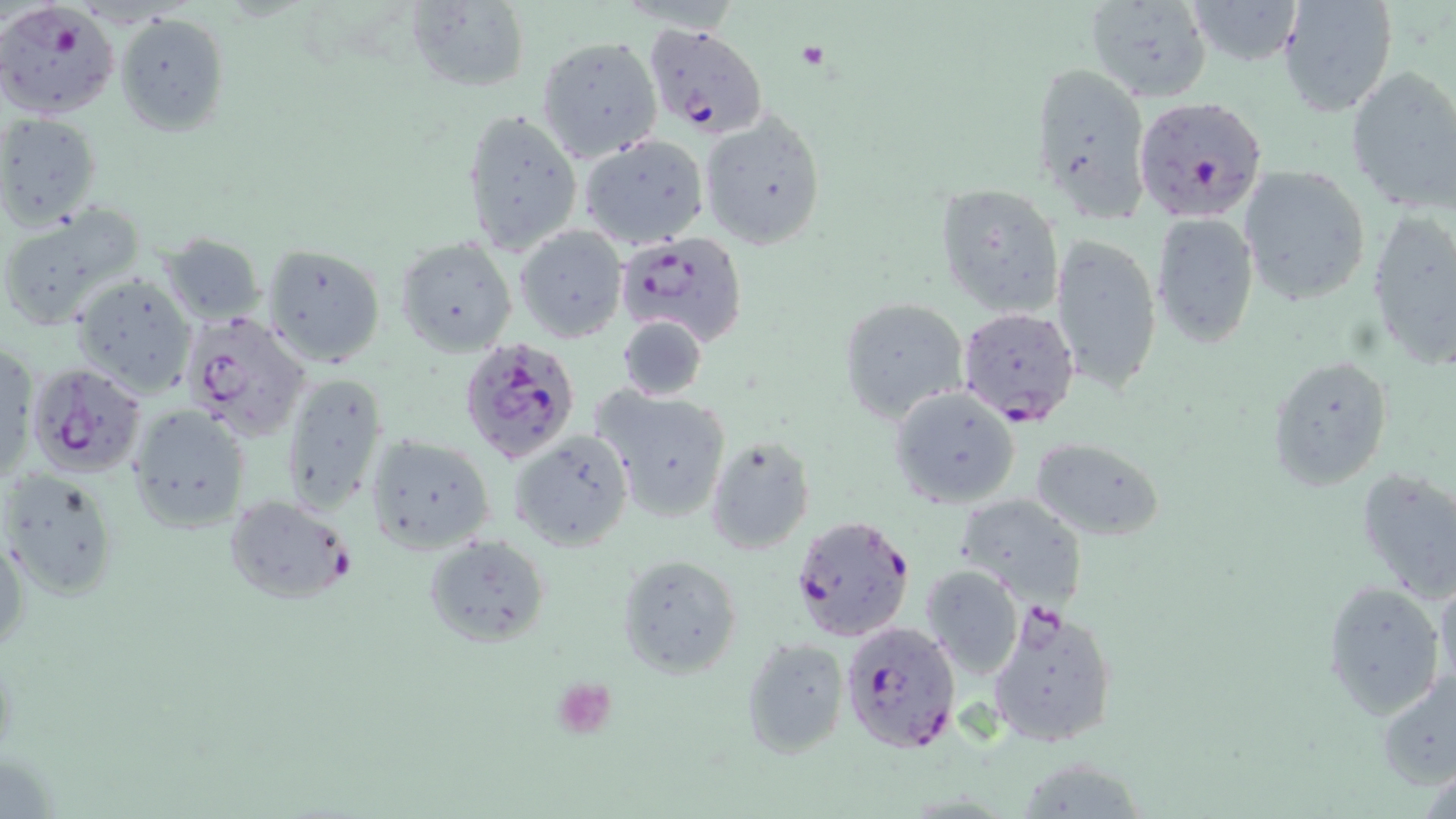
{
  "slide_level_diagnosis": "Plasmodium falciparum",
  "field_of_view": "one of a larger specimen",
  "preparation": "thin blood film",
  "plasmodium_falciparum_infected_red_blood_cell_locations": "approximate bounding boxes as (x1, y1, x2, y2) in pixels: (2, 3, 120, 119), (643, 23, 767, 139), (1133, 94, 1270, 222), (614, 231, 748, 347), (956, 305, 1081, 428), (179, 310, 313, 444), (458, 338, 581, 464), (26, 362, 148, 478), (224, 495, 356, 605), (790, 514, 916, 642), (987, 601, 1120, 749), (838, 619, 960, 754)",
  "magnification": "1000x",
  "uninfected_red_blood_cell_locations": "approximate bounding boxes as (x1, y1, x2, y2) in pixels: (404, 0, 531, 92), (1084, 0, 1213, 102), (1189, 1, 1303, 65), (1278, 1, 1396, 117), (115, 13, 231, 136), (537, 35, 663, 163), (1029, 59, 1152, 219), (1345, 65, 1456, 214), (461, 105, 583, 255), (1, 113, 102, 229), (701, 113, 827, 251), (578, 134, 710, 249), (1237, 163, 1372, 304), (935, 182, 1063, 319), (1, 208, 142, 333), (1366, 209, 1456, 373), (1151, 212, 1260, 348), (516, 226, 626, 341), (1049, 232, 1162, 391), (159, 233, 265, 326), (396, 236, 518, 357), (262, 242, 387, 369), (71, 272, 197, 398), (837, 297, 969, 424), (616, 315, 707, 403), (1, 346, 36, 486), (1268, 354, 1392, 490), (281, 375, 390, 515), (593, 387, 732, 524), (890, 388, 1019, 508), (128, 404, 252, 531), (510, 431, 633, 550), (366, 433, 495, 555), (705, 435, 814, 556), (1030, 436, 1165, 542), (1355, 465, 1456, 602), (1, 469, 120, 598), (957, 491, 1088, 606), (2, 532, 27, 656), (425, 536, 551, 646), (616, 555, 743, 677), (921, 564, 1024, 678), (1433, 569, 1456, 694), (1323, 580, 1446, 719), (741, 636, 850, 758), (1376, 666, 1456, 789), (1014, 758, 1151, 817)",
  "image_size": "1456×819 pixels",
  "modality": "light microscopy",
  "stain": "May-Grünwald-Giemsa"
}